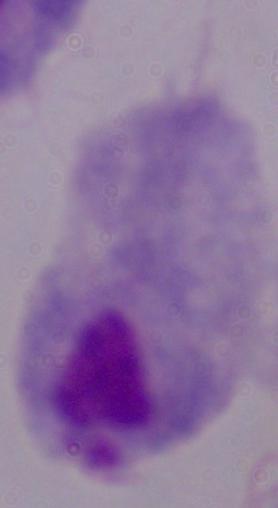

{
  "magnification": "1000x",
  "modality": "micrograph",
  "identification": "trichomonad"
}